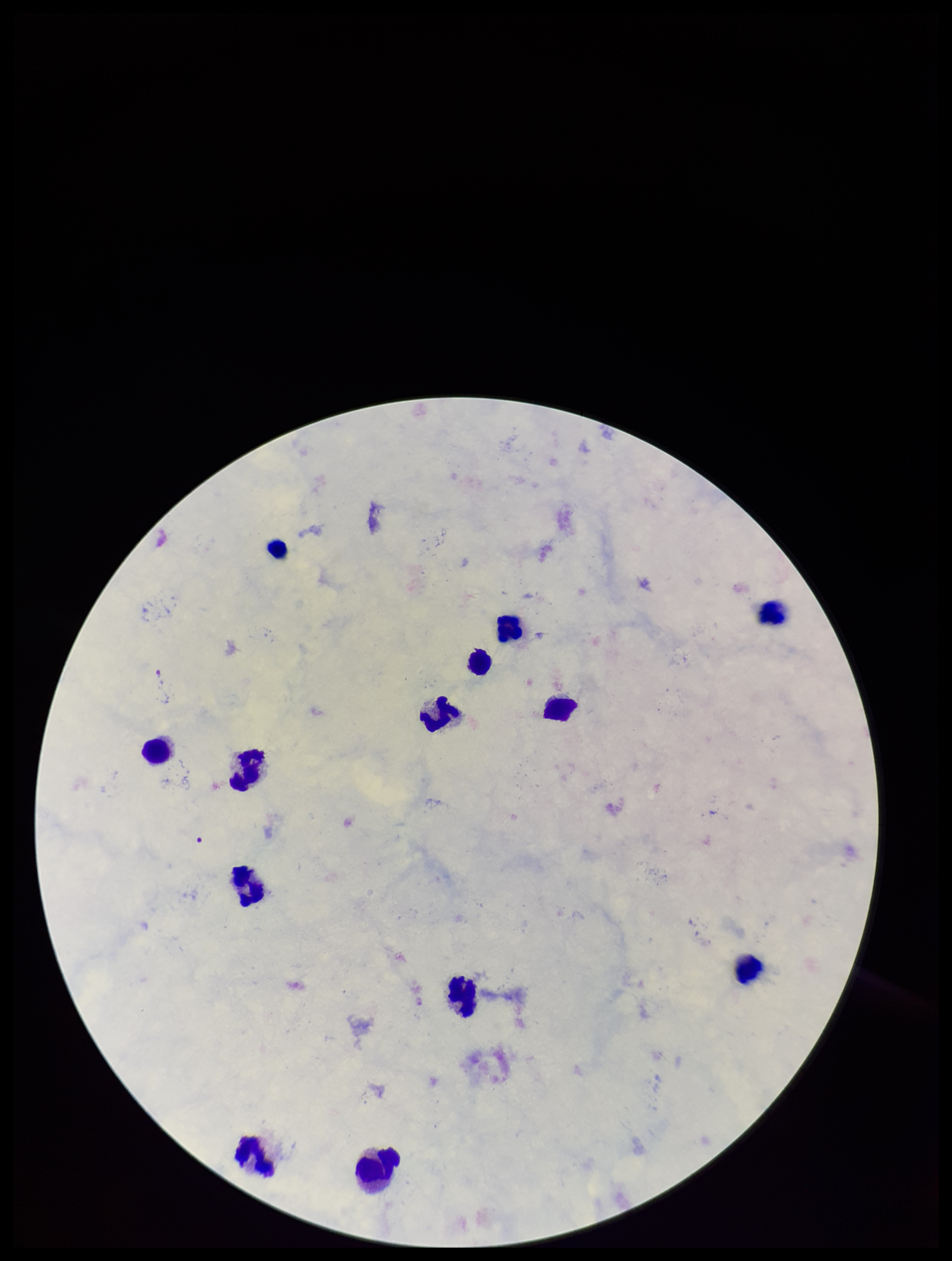

leukocyte count = 13
stain = Giemsa
capture = smartphone photograph through the microscope eyepiece
species reported for this patient = Plasmodium falciparum
parasite count = 0
field of view = single
patient malaria status = infected
preparation = thick blood smear
Plasmodium parasites = none detected
image size = 952×1261 pixels